Give the preparation type.
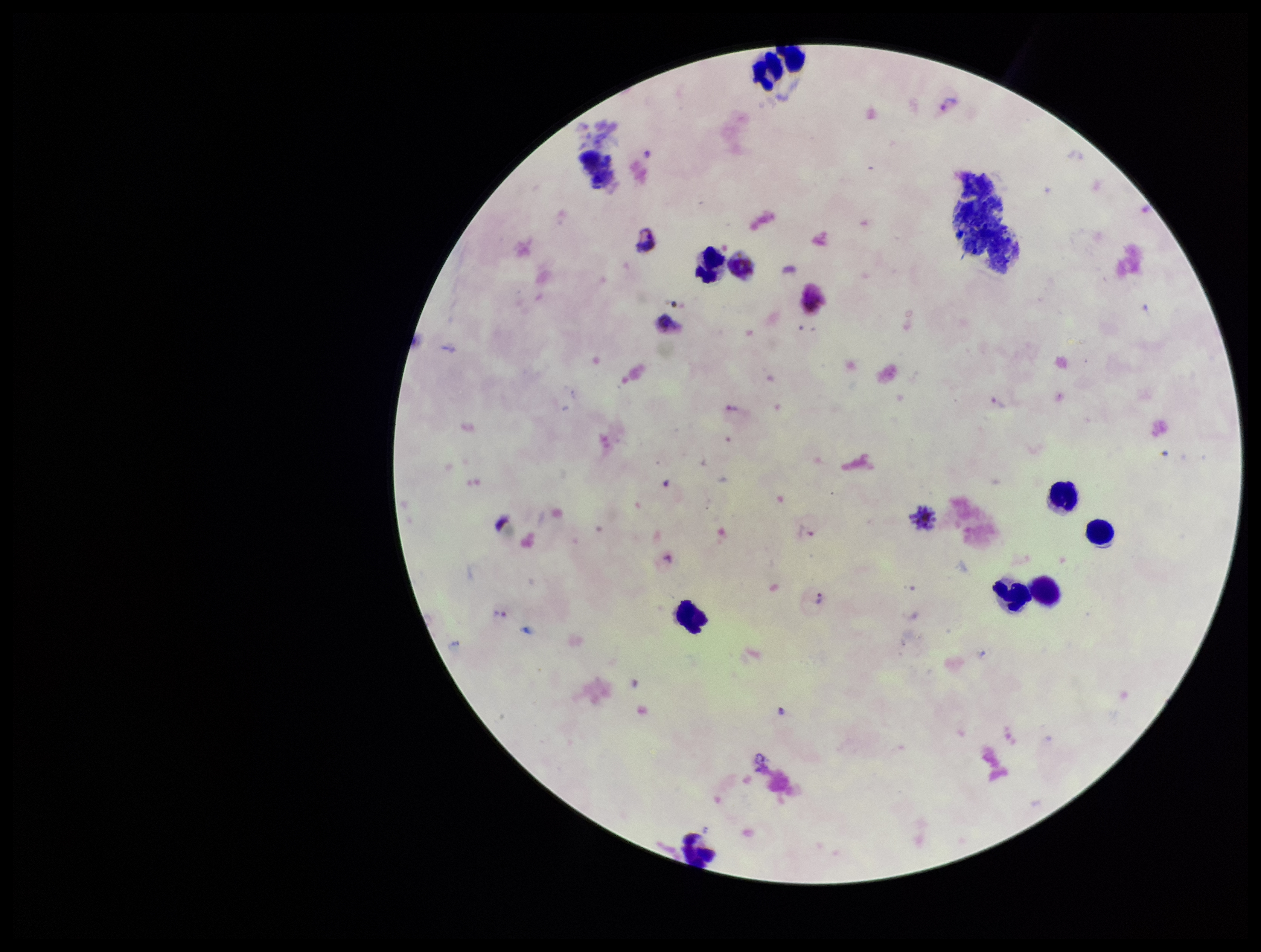

Thick.

Smartphone photograph taken through the eyepiece of a microscope. Stained with Giemsa. Single field of view. Plasmodium parasites: identified. Species reported for this patient: Plasmodium vivax. Image is 1261×952 pixels. Parasite count: 3. Patient malaria status: positive. Leukocyte count: 11.